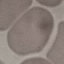
Malaria status: uninfected. Giemsa-stained preparation. Automatically extracted cell patch, resized to 64 × 64 pixels. Acquired by smartphone through the microscope eyepiece. Thin blood film.